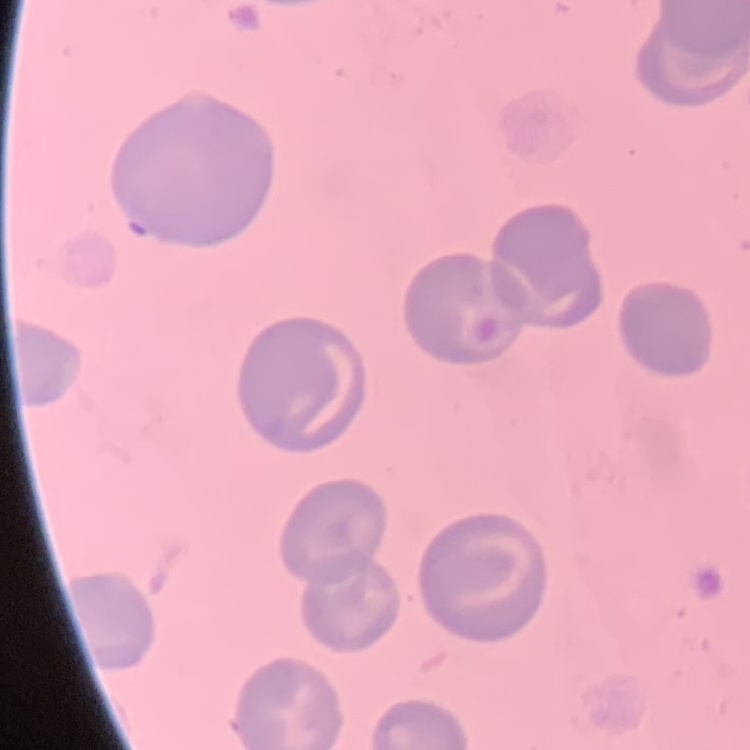
The red blood cells exhibit no rouleaux formation. Thin blood film. Field's or Giemsa stain. One tile cut from a larger photomicrograph.